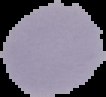
Summary:
  - Image type: cell region segmented out of the field of view; surrounding area masked to black
  - Result: no Plasmodium parasites detected
  - Preparation: thin blood film
  - Image size: 106×97 pixels